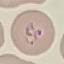

Result: malaria parasites identified. Photographed with a smartphone camera at the microscope eyepiece. Thin smear of blood. Cell patch, automatically extracted from a larger field of view and resized to 64 × 64 pixels. Giemsa stain.